Comment on the morphology of the erythrocytes.
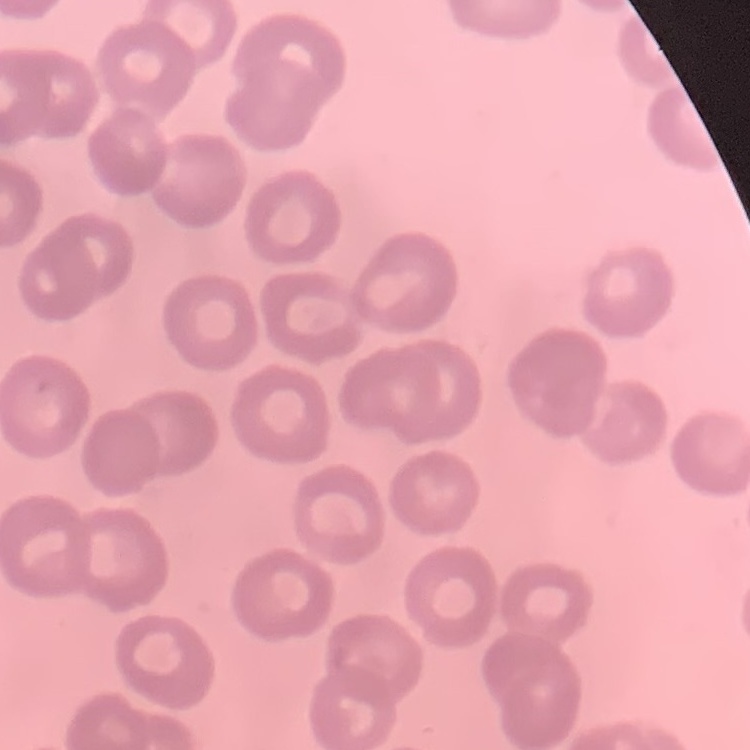

They show no rouleaux formation.

preparation = thin peripheral smear
stain = Field's or Giemsa
image type = one tile cut from a larger photomicrograph